Locate the red blood cells and classify each one as Plasmodium falciparum-infected, uninfected, or of indeterminate infection status.
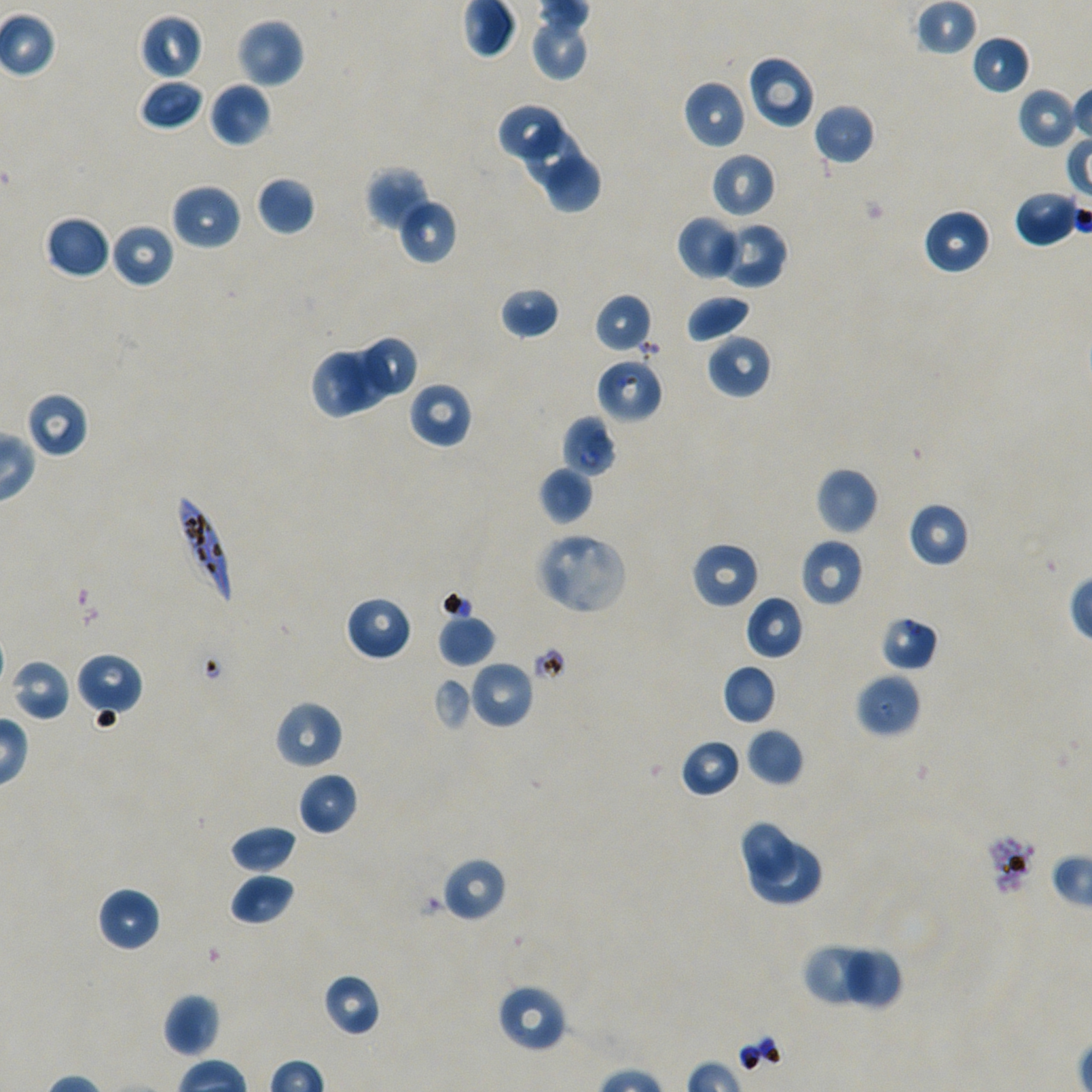
Approximate bounding boxes as [x1, y1, x2, y2] in pixels. Not every red blood cell is marked.
Infected red blood cells: [174, 491, 234, 608].
Red blood cells of indeterminate infection status: [595, 357, 664, 423], [561, 414, 617, 477], [879, 615, 939, 672], [855, 672, 922, 738], [983, 831, 1038, 898].
Uninfected red blood cells: [916, 0, 979, 56], [139, 14, 202, 80], [532, 16, 590, 81], [236, 18, 305, 88], [970, 34, 1031, 94], [746, 54, 815, 129], [139, 79, 204, 131], [682, 79, 747, 150], [208, 81, 270, 147], [1017, 86, 1079, 148], [499, 103, 565, 161], [813, 103, 875, 166], [522, 128, 583, 187], [710, 151, 776, 219], [546, 156, 602, 213], [364, 165, 433, 232], [255, 175, 316, 236], [171, 183, 242, 251], [1013, 188, 1081, 247], [399, 198, 458, 264], [922, 208, 990, 275], [43, 215, 111, 280], [676, 215, 742, 280], [715, 221, 788, 289], [111, 222, 175, 289], [500, 286, 561, 340], [594, 293, 653, 353], [686, 294, 752, 344], [706, 332, 772, 399], [362, 334, 420, 393], [337, 349, 390, 413], [310, 352, 367, 418], [407, 382, 473, 449], [24, 390, 90, 458], [538, 466, 594, 526], [816, 467, 879, 535], [907, 501, 970, 568], [534, 532, 627, 615], [800, 538, 864, 608], [690, 541, 760, 609], [346, 595, 413, 661], [744, 595, 804, 661], [438, 614, 496, 668], [75, 653, 143, 721], [9, 658, 72, 722], [469, 659, 534, 729], [722, 664, 778, 725], [432, 678, 473, 731], [273, 699, 343, 770], [746, 727, 805, 786], [680, 738, 743, 798], [297, 771, 358, 837], [738, 819, 799, 883], [230, 824, 297, 875], [748, 843, 820, 904], [440, 856, 508, 923], [230, 873, 295, 926], [96, 886, 160, 952], [801, 943, 881, 1009], [838, 945, 905, 1010], [322, 973, 381, 1037], [496, 983, 568, 1053], [163, 993, 221, 1058].

preparation: thin blood film
culture: in-vitro Plasmodium falciparum strain NF54, static
field_of_view: one from this slide
donor_blood_group: A+/O+
objective: 100x, oil immersion, numerical aperture 1.45
image_size: 1092×1092 pixels
stain: Giemsa